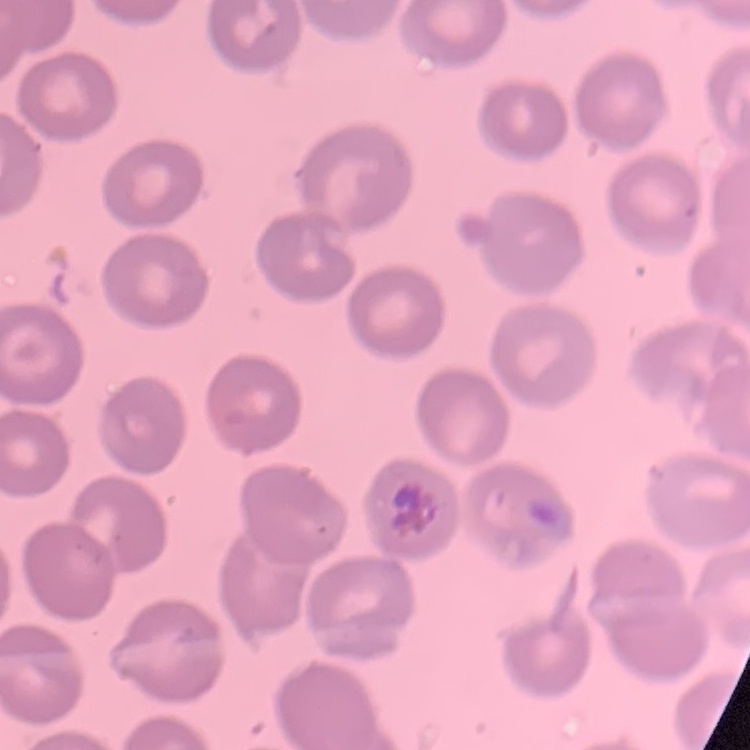
red_blood_cell_morphology: no rouleaux formation
stain: Field's or Giemsa
preparation: thin peripheral smear
image_type: square crop of a larger photomicrograph